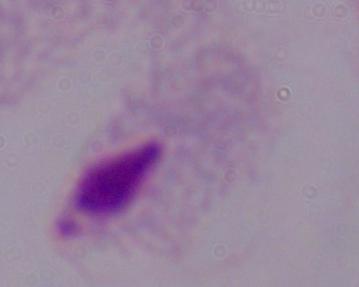

A trichomonad is shown. Captured at 1000x magnification. Micrograph.